State the blood parasite species.
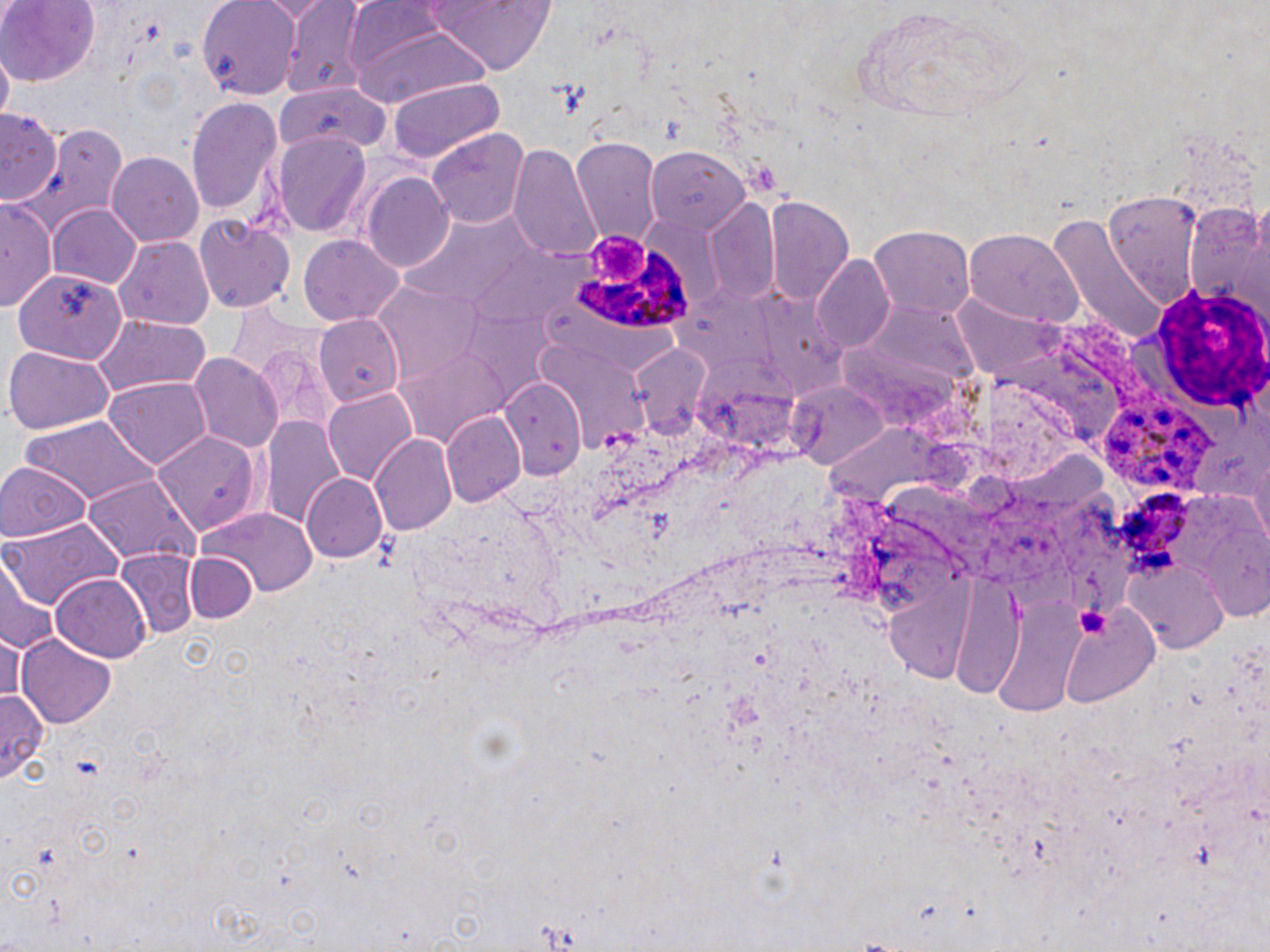

Plasmodium ovale.

Summary:
  - Coordinate format: approximate bounding boxes as named x1/y1/x2/y2 corners in pixels
  - Platelet locations: (x1=590, y1=234, x2=648, y2=282), (x1=1078, y1=608, x2=1111, y2=639)
  - Plasmodium ovale-infected red blood cell locations: (x1=575, y1=250, x2=695, y2=330), (x1=1099, y1=401, x2=1225, y2=499)
  - White blood cell locations: (x1=1151, y1=287, x2=1269, y2=412)
  - Uninfected red blood cell locations: (x1=0, y1=0, x2=100, y2=84), (x1=198, y1=0, x2=302, y2=100), (x1=256, y1=1, x2=333, y2=22), (x1=416, y1=2, x2=561, y2=73), (x1=281, y1=4, x2=369, y2=97), (x1=352, y1=21, x2=485, y2=109), (x1=386, y1=76, x2=504, y2=164), (x1=274, y1=82, x2=384, y2=155), (x1=186, y1=95, x2=282, y2=217), (x1=1, y1=105, x2=63, y2=209), (x1=15, y1=123, x2=125, y2=238), (x1=427, y1=127, x2=528, y2=232), (x1=276, y1=133, x2=371, y2=237), (x1=572, y1=138, x2=660, y2=250), (x1=512, y1=143, x2=598, y2=261), (x1=644, y1=145, x2=750, y2=234), (x1=109, y1=153, x2=203, y2=247), (x1=361, y1=173, x2=453, y2=271), (x1=1100, y1=190, x2=1203, y2=304), (x1=763, y1=194, x2=853, y2=304), (x1=1, y1=195, x2=58, y2=313), (x1=704, y1=201, x2=780, y2=303), (x1=1184, y1=201, x2=1270, y2=327), (x1=48, y1=202, x2=144, y2=289), (x1=1048, y1=213, x2=1164, y2=346), (x1=196, y1=215, x2=294, y2=315), (x1=401, y1=215, x2=542, y2=313), (x1=870, y1=226, x2=974, y2=317), (x1=964, y1=229, x2=1082, y2=324), (x1=115, y1=235, x2=212, y2=332), (x1=298, y1=235, x2=404, y2=326), (x1=811, y1=256, x2=893, y2=352), (x1=13, y1=267, x2=131, y2=367), (x1=371, y1=278, x2=487, y2=392), (x1=754, y1=284, x2=851, y2=401), (x1=668, y1=287, x2=781, y2=373), (x1=956, y1=295, x2=1067, y2=382), (x1=866, y1=303, x2=982, y2=390), (x1=462, y1=304, x2=563, y2=405), (x1=226, y1=306, x2=322, y2=379), (x1=311, y1=311, x2=407, y2=403), (x1=90, y1=314, x2=211, y2=398), (x1=533, y1=336, x2=649, y2=454), (x1=834, y1=344, x2=963, y2=430), (x1=629, y1=345, x2=715, y2=441), (x1=4, y1=346, x2=113, y2=433), (x1=388, y1=350, x2=512, y2=452), (x1=189, y1=352, x2=282, y2=452), (x1=694, y1=357, x2=798, y2=457), (x1=498, y1=376, x2=586, y2=479), (x1=787, y1=376, x2=891, y2=469), (x1=103, y1=378, x2=211, y2=471), (x1=324, y1=388, x2=418, y2=486), (x1=443, y1=411, x2=525, y2=507), (x1=261, y1=414, x2=346, y2=524), (x1=20, y1=417, x2=157, y2=505), (x1=825, y1=418, x2=972, y2=510), (x1=154, y1=430, x2=262, y2=532), (x1=371, y1=435, x2=460, y2=534), (x1=1249, y1=446, x2=1269, y2=553), (x1=0, y1=461, x2=89, y2=543), (x1=300, y1=473, x2=389, y2=564), (x1=83, y1=474, x2=198, y2=565), (x1=196, y1=508, x2=319, y2=597), (x1=4, y1=517, x2=123, y2=617), (x1=1193, y1=517, x2=1270, y2=627), (x1=112, y1=548, x2=200, y2=644), (x1=188, y1=550, x2=262, y2=623), (x1=1, y1=558, x2=57, y2=659), (x1=1132, y1=561, x2=1227, y2=654), (x1=882, y1=564, x2=976, y2=686), (x1=953, y1=564, x2=1022, y2=703), (x1=51, y1=571, x2=152, y2=661), (x1=996, y1=589, x2=1081, y2=725), (x1=1055, y1=596, x2=1158, y2=710), (x1=0, y1=629, x2=28, y2=708), (x1=18, y1=633, x2=118, y2=729), (x1=0, y1=689, x2=45, y2=785)
  - Magnification: 1000x
  - Preparation: thin blood film
  - Stain: May-Grünwald-Giemsa
  - Field of view: one of a larger specimen
  - Image size: 1270×952 pixels
  - Modality: light microscopy